Report the malaria status of this cell.
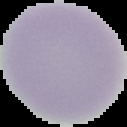

Uninfected.

Image is 127×127 pixels. From a thin blood film. Cell region segmented out of the field of view; the surrounding area is masked to black.